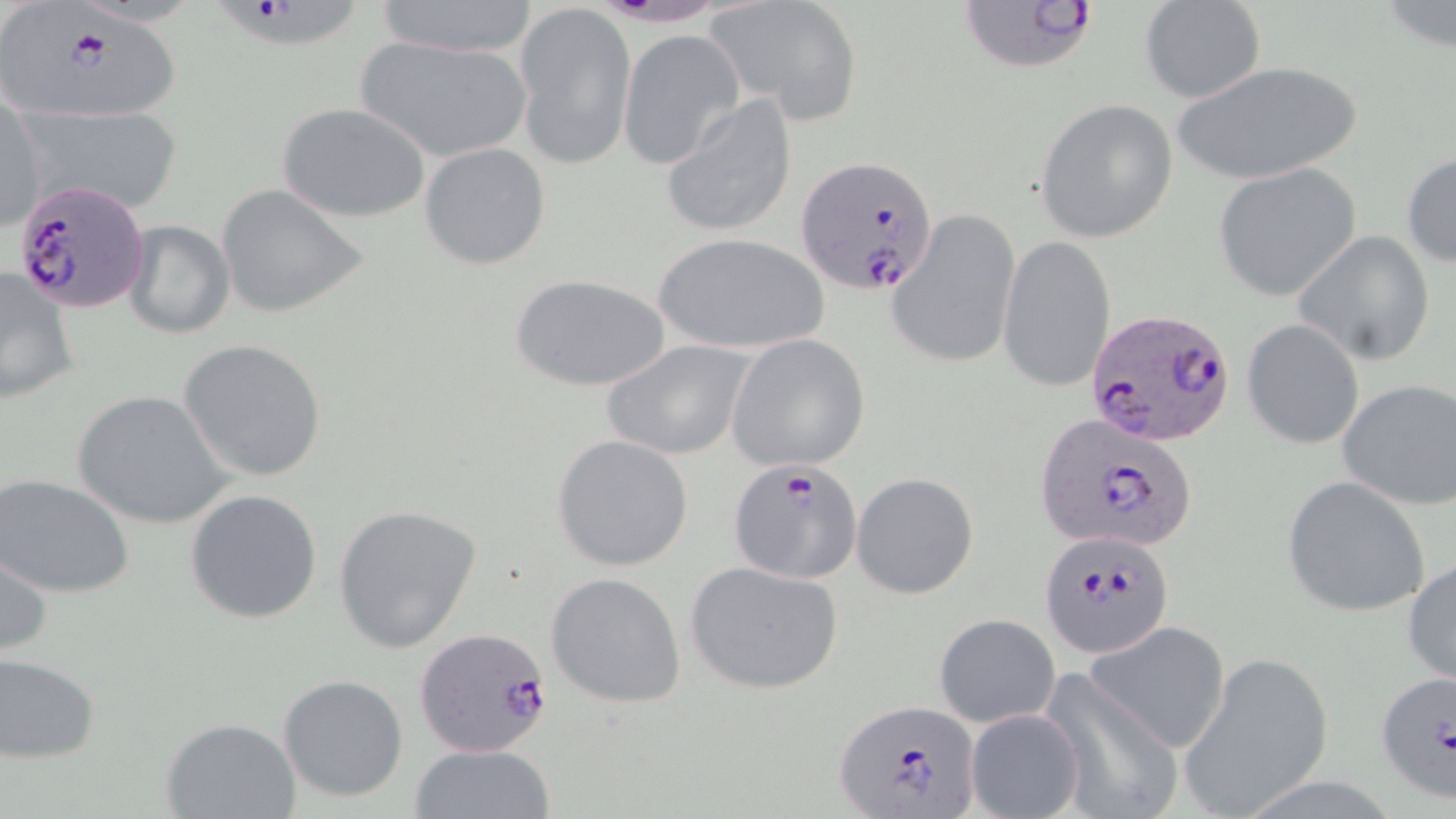

Approximate bounding boxes as named x1/y1/x2/y2 corners in pixels. Uninfected red blood cell locations: (x1=374, y1=0, x2=541, y2=61), (x1=712, y1=0, x2=864, y2=120), (x1=1139, y1=0, x2=1267, y2=105), (x1=512, y1=2, x2=636, y2=169), (x1=619, y1=31, x2=743, y2=167), (x1=353, y1=33, x2=533, y2=164), (x1=1172, y1=61, x2=1365, y2=186), (x1=661, y1=93, x2=800, y2=239), (x1=1, y1=95, x2=46, y2=233), (x1=1035, y1=99, x2=1177, y2=243), (x1=278, y1=102, x2=431, y2=223), (x1=21, y1=105, x2=183, y2=216), (x1=418, y1=142, x2=552, y2=269), (x1=1402, y1=151, x2=1455, y2=270), (x1=1213, y1=165, x2=1361, y2=301), (x1=217, y1=184, x2=369, y2=317), (x1=887, y1=208, x2=1020, y2=371), (x1=121, y1=220, x2=235, y2=339), (x1=1292, y1=230, x2=1436, y2=365), (x1=651, y1=234, x2=831, y2=356), (x1=998, y1=235, x2=1116, y2=394), (x1=0, y1=264, x2=79, y2=407), (x1=512, y1=273, x2=670, y2=393), (x1=1242, y1=320, x2=1365, y2=449), (x1=726, y1=333, x2=871, y2=471), (x1=178, y1=339, x2=327, y2=481), (x1=600, y1=339, x2=755, y2=460), (x1=1337, y1=379, x2=1456, y2=510), (x1=73, y1=390, x2=233, y2=528), (x1=551, y1=434, x2=696, y2=571), (x1=851, y1=472, x2=979, y2=600), (x1=0, y1=473, x2=135, y2=599), (x1=1281, y1=475, x2=1432, y2=617), (x1=184, y1=487, x2=323, y2=623), (x1=332, y1=503, x2=484, y2=653), (x1=1, y1=543, x2=52, y2=664), (x1=1404, y1=554, x2=1456, y2=692), (x1=684, y1=559, x2=845, y2=694), (x1=546, y1=571, x2=687, y2=707), (x1=933, y1=613, x2=1060, y2=727), (x1=1084, y1=622, x2=1231, y2=753), (x1=1176, y1=648, x2=1335, y2=819), (x1=0, y1=650, x2=101, y2=762), (x1=1038, y1=669, x2=1182, y2=819), (x1=278, y1=673, x2=409, y2=803), (x1=965, y1=707, x2=1084, y2=819), (x1=160, y1=717, x2=302, y2=819), (x1=411, y1=742, x2=554, y2=819). Plasmodium falciparum-infected red blood cell locations: (x1=1, y1=0, x2=178, y2=127), (x1=217, y1=0, x2=362, y2=52), (x1=960, y1=1, x2=1101, y2=77), (x1=794, y1=154, x2=939, y2=293), (x1=15, y1=177, x2=150, y2=311), (x1=1086, y1=311, x2=1238, y2=449), (x1=1032, y1=413, x2=1201, y2=553), (x1=726, y1=458, x2=863, y2=582), (x1=1040, y1=532, x2=1172, y2=657), (x1=416, y1=629, x2=555, y2=761), (x1=1373, y1=670, x2=1455, y2=805), (x1=833, y1=698, x2=984, y2=817). Slide-level diagnosis: Plasmodium falciparum. Captured at 1000x magnification. Image is 1456×819 pixels. One field of a larger specimen. May-Grünwald-Giemsa stain. Light microscopy. Thin blood smear.